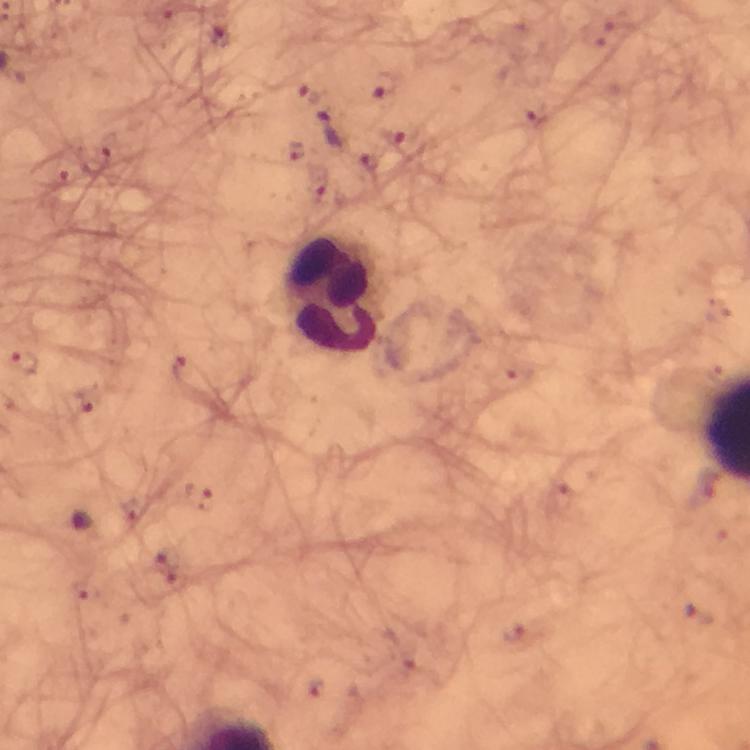

capture = smartphone photograph through a microscope
leukocyte locations = approximate centers as (x, y) in pixels: (333, 296)
magnification = 100x
stain = Giemsa
cropped from = one field of view
Plasmodium parasite locations = approximate centers as (x, y) in pixels: (219, 35), (384, 86), (332, 128), (400, 133), (371, 161), (23, 364), (179, 368), (86, 401)
context = from a diagnostic examination for malaria
image size = 750×750 pixels
immersion oil = applied
preparation = thick smear